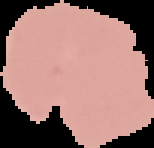
Summary:
  - Image type: cell region segmented out of the field of view; surrounding area masked to black
  - Image size: 154×148 pixels
  - Result: negative for Plasmodium parasites
  - Preparation: thin blood smear